Describe the morphology of the red blood cells.
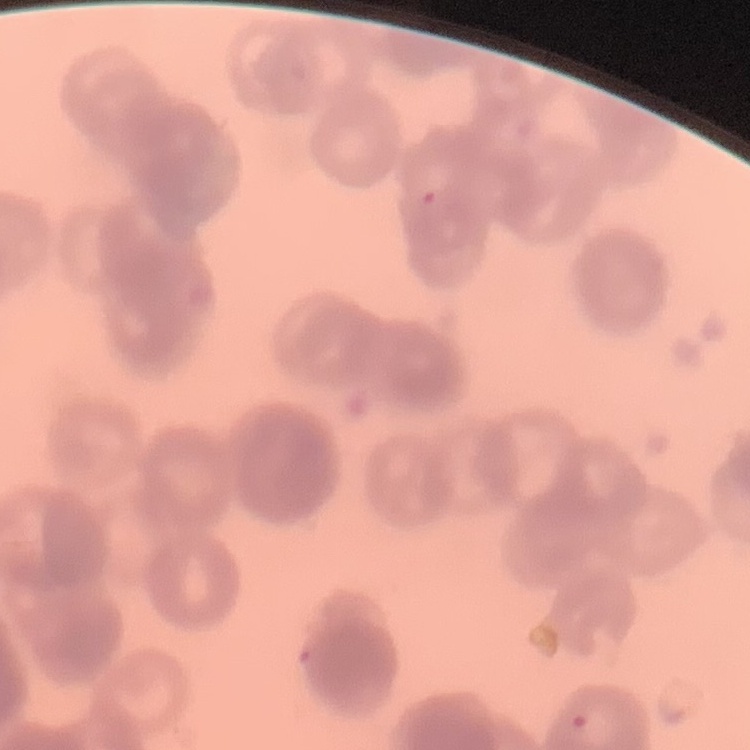
They show rouleaux formation.

stain: Field's or Giemsa
image_type: square crop of a larger photomicrograph
preparation: thin peripheral smear